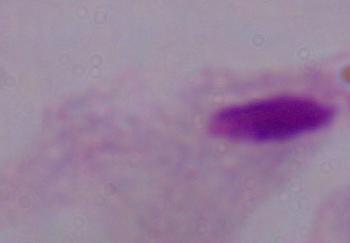

{
  "magnification": "1000x",
  "identification": "trichomonad",
  "modality": "micrograph"
}